Assess the morphology of the erythrocytes.
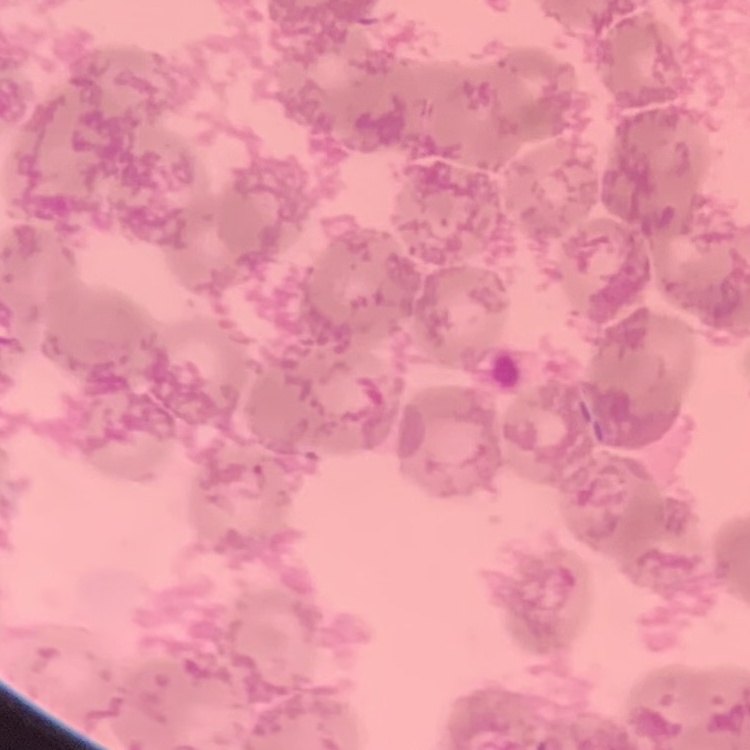

They show rouleaux formation.

preparation = thin peripheral smear
image type = one tile cut from a larger photomicrograph
stain = Field's or Giemsa